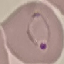
malaria status = parasitized
preparation = thin smear
stain = Giemsa
image type = cell patch, automatically extracted from a larger field of view and resized to 64 × 64 pixels
capture = smartphone through the microscope eyepiece